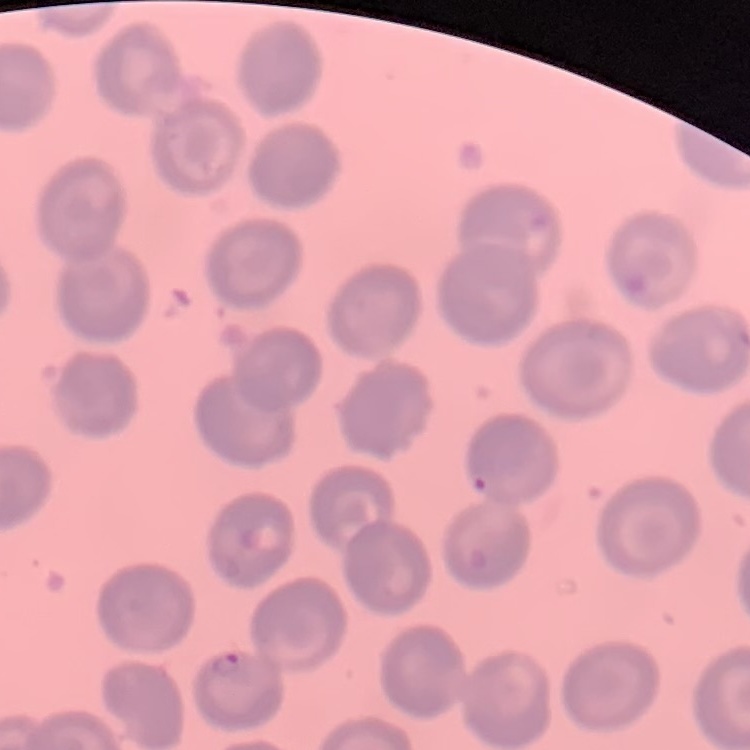

The red blood cells show no rouleaux formation. Stained with either Field's or Giemsa. Square crop of a larger photomicrograph. Thin blood film.